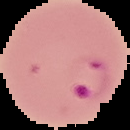

Image is 130×130 pixels. Result: malaria parasites detected. From a thin blood film. The area outside the segmented cell region is set to black.